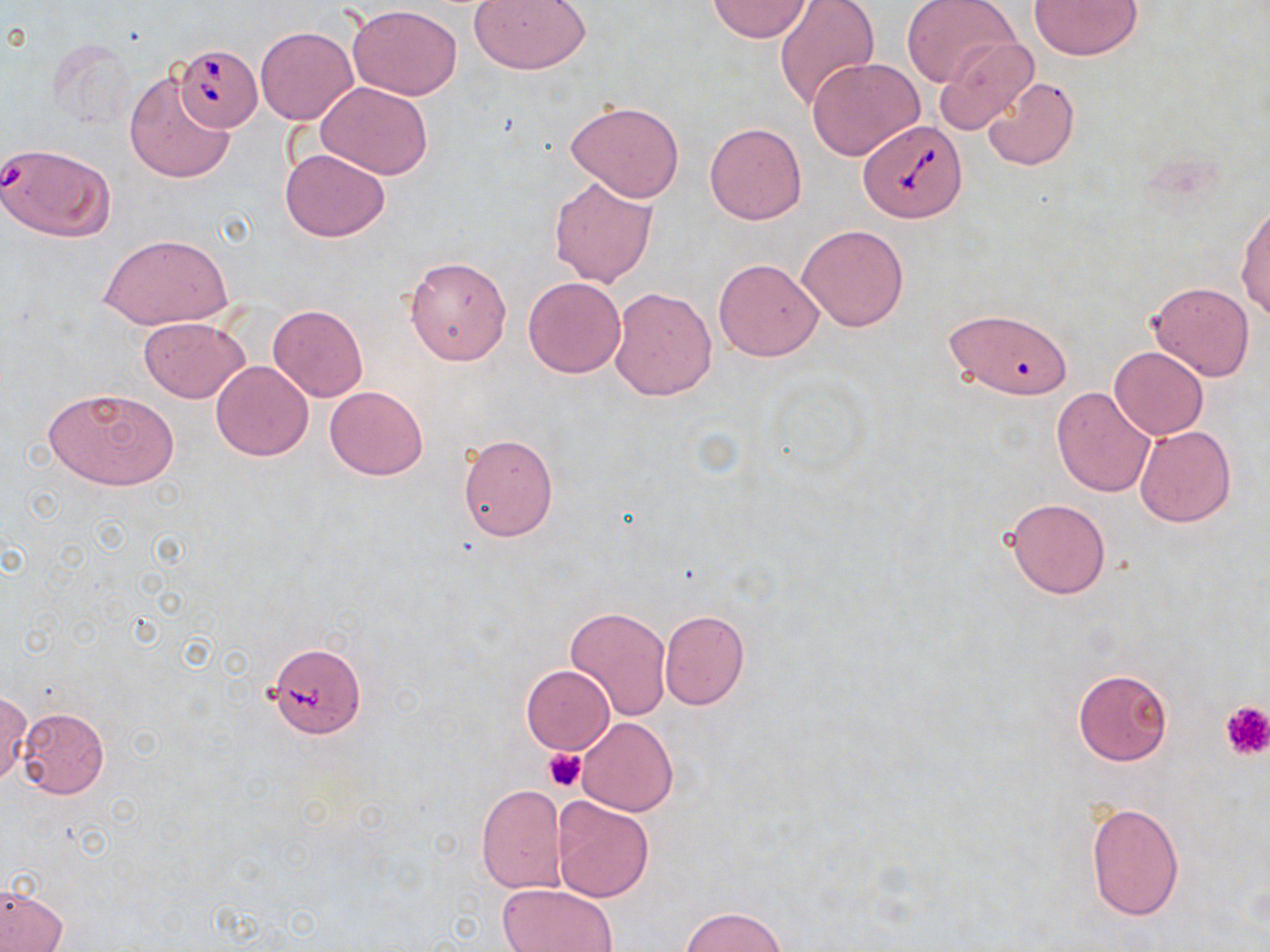 Approximate bounding boxes as (x1,y1)-(x2,y2) corner pairs in pixels. Uninfected red blood cell locations: (469,0)-(591,73), (773,0)-(879,111), (902,0)-(1020,90), (1029,0)-(1144,59), (705,1)-(813,42), (346,4)-(463,100), (255,26)-(357,125), (934,37)-(1039,135), (46,39)-(136,132), (808,56)-(924,159), (124,71)-(233,183), (982,76)-(1081,171), (314,81)-(435,182), (565,103)-(685,202), (705,122)-(807,224), (281,147)-(389,242), (548,175)-(659,287), (1236,200)-(1270,323), (797,224)-(909,333), (101,233)-(231,330), (404,254)-(512,366), (713,258)-(824,361), (523,277)-(626,378), (1145,280)-(1256,382), (608,286)-(716,402), (267,303)-(368,402), (941,307)-(1074,402), (137,316)-(251,404), (1108,346)-(1209,440), (210,361)-(314,460), (43,386)-(180,490), (325,386)-(428,479), (1051,386)-(1156,496), (1133,425)-(1237,528), (456,431)-(558,542), (1004,497)-(1111,599), (565,607)-(671,721), (659,610)-(749,709), (521,665)-(614,755), (1072,668)-(1172,766), (0,692)-(32,784), (16,706)-(110,799), (578,717)-(677,816), (475,784)-(568,893), (551,796)-(655,902), (1085,801)-(1185,921), (497,882)-(618,952), (1,886)-(68,952), (680,906)-(786,952). Platelet locations: (1218,699)-(1270,760), (543,747)-(588,791). Babesia divergens-infected red blood cell locations: (173,44)-(263,131), (857,120)-(966,223), (0,140)-(116,241), (264,642)-(367,736). Slide-level diagnosis: Babesia divergens. One field of a larger specimen. Thin blood smear. Optical microscopy. Image is 1270×952 pixels. Captured at 1000x magnification. May-Grünwald-Giemsa stain.